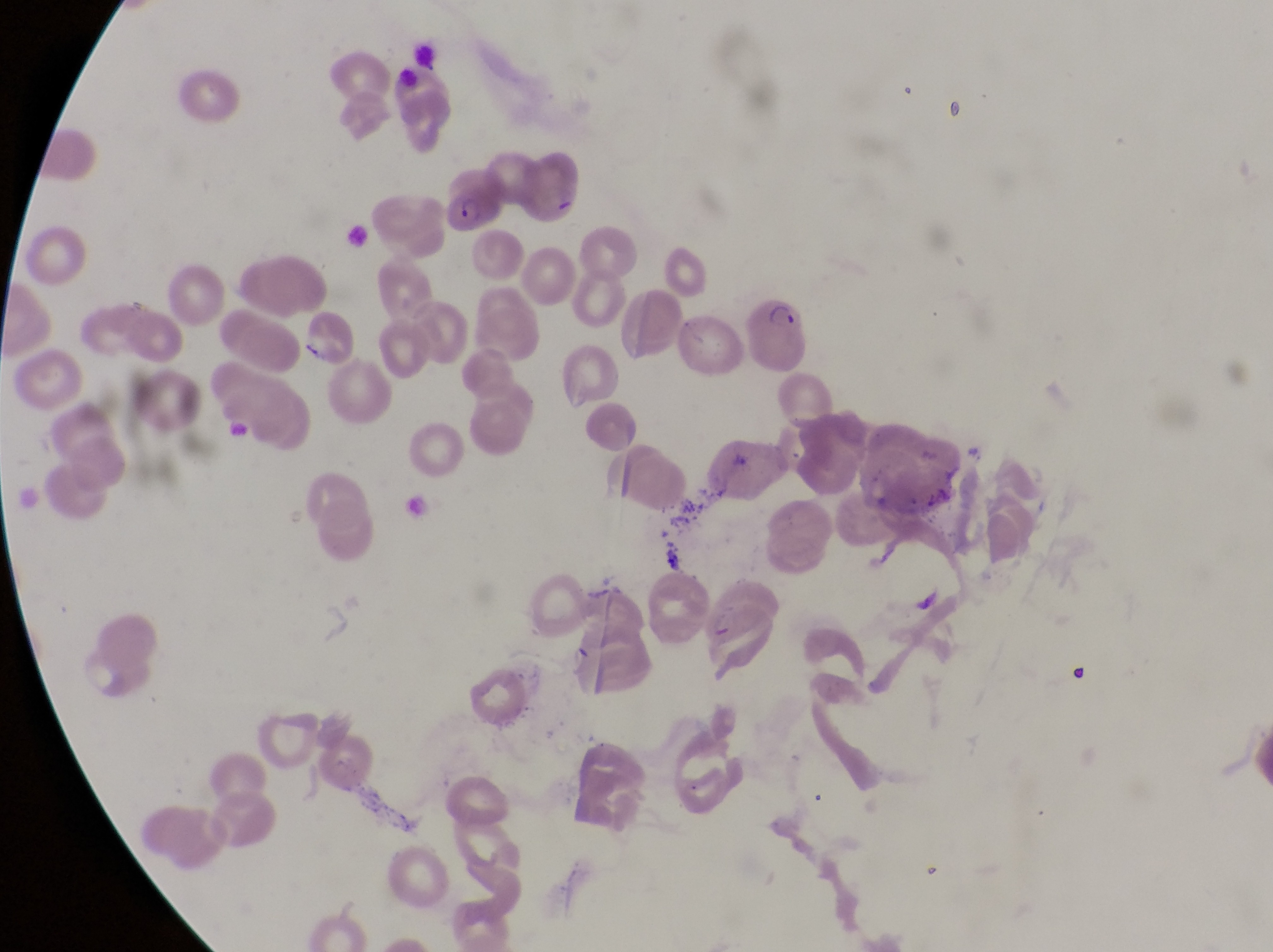
Approximate bounding boxes as [left, top, right, bottom] in pixels. Parasitised red blood cell locations: [445, 168, 502, 229], [746, 290, 809, 373]. Single field of view. Thin blood smear. Sample from Uganda. Magnification of 1000x. Image is 1273×952 pixels. Captured by a smartphone held over the eyepiece of an Olympus CX-23 microscope.